Give the extent of all Plasmodium falciparum-infected red blood cells.
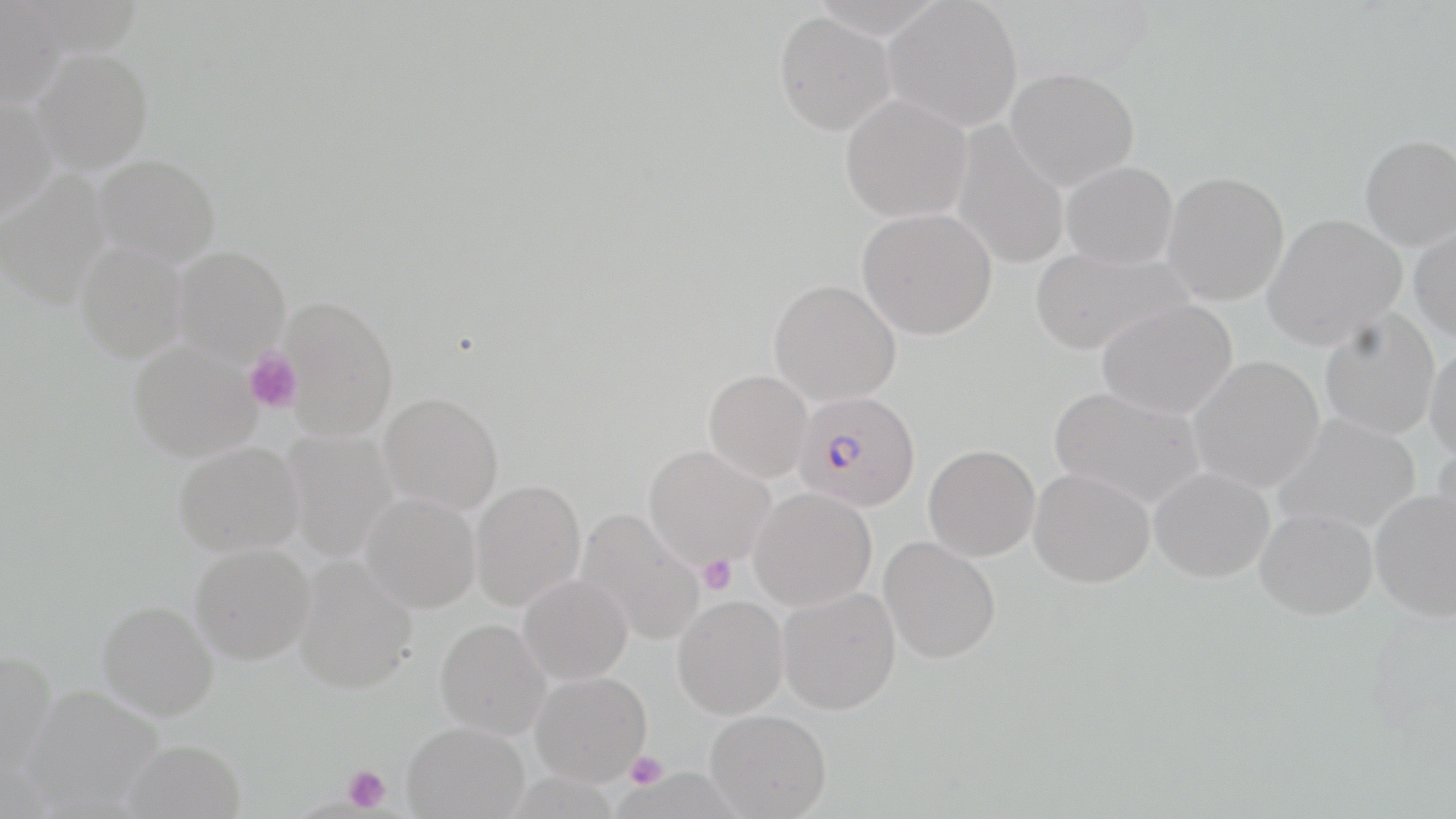

Approximate bounding boxes as (x1,y1)-(x2,y2) corner pairs in pixels.
Plasmodium falciparum-infected red blood cells: (792,391)-(920,512).

Platelet locations: (243,347)-(303,414), (696,554)-(738,595), (623,752)-(668,789), (342,764)-(391,813). Uninfected red blood cell locations: (0,0)-(66,109), (807,0)-(945,39), (883,1)-(1023,133), (774,12)-(896,136), (30,47)-(153,173), (1005,67)-(1139,191), (840,94)-(972,224), (0,98)-(56,220), (951,122)-(1069,270), (1359,134)-(1456,250), (94,154)-(220,266), (1061,161)-(1178,269), (0,172)-(111,310), (1162,172)-(1290,305), (857,208)-(997,340), (1262,213)-(1406,349), (1409,226)-(1456,344), (74,241)-(188,362), (1028,244)-(1192,357), (173,246)-(290,365), (768,279)-(901,406), (280,296)-(399,440), (1097,299)-(1238,419), (1318,311)-(1441,440), (127,340)-(260,462), (1425,343)-(1456,463), (1188,355)-(1325,493), (703,370)-(813,483), (1049,385)-(1205,509), (378,392)-(504,515), (1273,413)-(1421,535), (281,429)-(397,561), (173,441)-(303,556), (1430,443)-(1456,560), (923,444)-(1040,561), (643,445)-(775,570), (1028,467)-(1155,588), (1149,467)-(1274,582), (470,480)-(586,611), (748,488)-(876,611), (1369,490)-(1456,622), (360,492)-(480,612), (575,507)-(705,646), (1254,507)-(1377,620), (879,536)-(1001,664), (189,543)-(315,665), (293,554)-(418,693), (518,574)-(633,684), (777,587)-(901,715), (673,596)-(788,718), (97,600)-(219,720), (435,618)-(551,739), (0,650)-(58,778), (530,671)-(651,785), (24,684)-(164,813), (705,710)-(832,818), (402,721)-(529,818), (121,739)-(246,819). Slide-level diagnosis: Plasmodium falciparum. Thin blood film. 1000x magnification. May-Grünwald-Giemsa-stained preparation. Optical microscopy. Image is 1456×819 pixels. Single field of view.